Assess the morphology of the red blood cells.
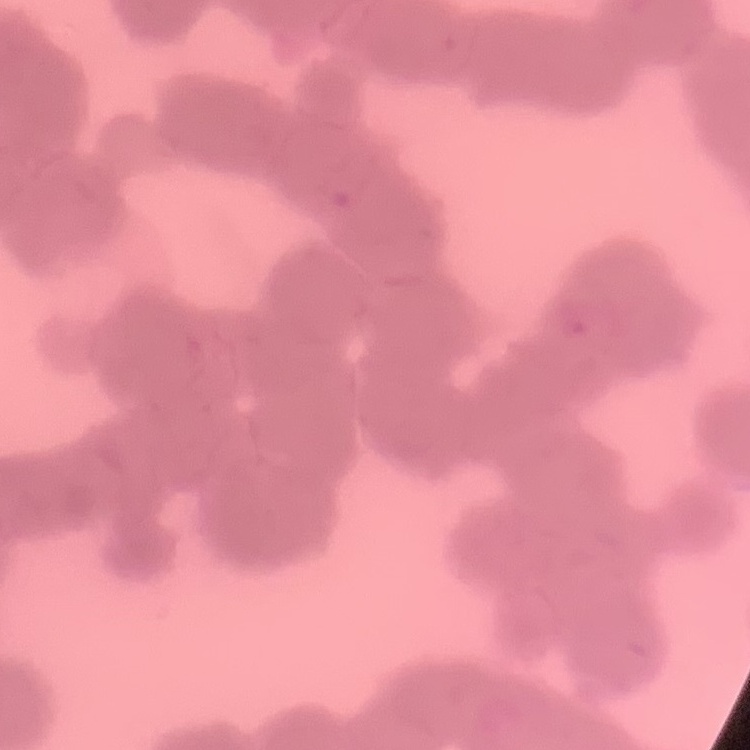

Rouleaux formation.

stain: Field's or Giemsa
image_type: square crop of a larger photomicrograph
preparation: thin blood smear